Outline each Plasmodium vivax-infected red blood cell.
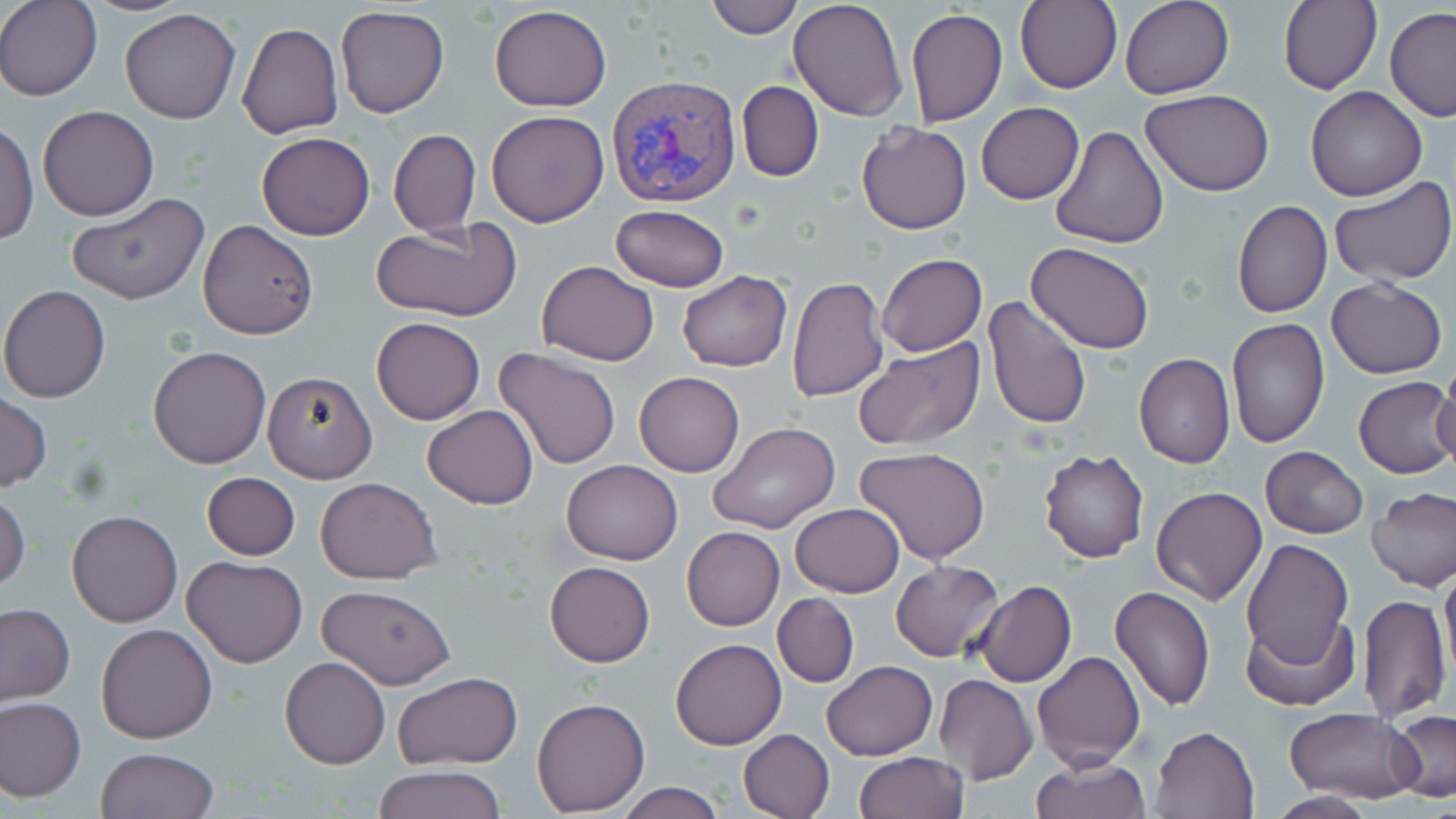
Approximate bounding boxes as (x1,y1)-(x2,y2) corner pairs in pixels.
Plasmodium vivax-infected red blood cells: (608,75)-(739,208).

slide-level diagnosis = Plasmodium vivax
field of view = single
uninfected red blood cell locations = approximate bounding boxes as (x1,y1)-(x2,y2) corner pairs in pixels: (0,0)-(101,101), (703,0)-(804,39), (788,0)-(909,121), (1120,0)-(1234,99), (1015,1)-(1122,94), (1279,1)-(1381,94), (336,5)-(450,118), (489,5)-(612,112), (1384,7)-(1456,122), (120,8)-(240,124), (906,9)-(1008,126), (238,21)-(345,140), (736,80)-(824,183), (1305,86)-(1428,201), (1141,90)-(1275,196), (976,103)-(1085,204), (38,105)-(160,220), (486,110)-(609,227), (0,118)-(38,248), (857,122)-(972,235), (1049,126)-(1168,249), (388,129)-(480,235), (256,132)-(375,241), (1330,176)-(1455,286), (66,192)-(210,307), (1232,200)-(1332,318), (612,205)-(730,292), (197,219)-(318,339), (370,223)-(521,320), (1026,241)-(1156,355), (877,253)-(986,357), (537,261)-(659,365), (678,271)-(791,371), (787,276)-(888,401), (1326,277)-(1448,379), (1,283)-(113,402), (981,295)-(1094,432), (1227,316)-(1330,449), (371,317)-(484,425), (854,336)-(985,451), (149,345)-(271,468), (493,347)-(622,472), (1134,354)-(1235,468), (1431,367)-(1456,473), (261,369)-(379,483), (633,371)-(745,476), (1353,375)-(1456,479), (0,392)-(51,493), (422,404)-(538,510), (710,422)-(841,533), (854,446)-(991,566), (1261,446)-(1368,539), (1039,449)-(1149,562), (560,460)-(684,565), (202,472)-(300,560), (315,477)-(442,584), (1151,487)-(1267,606), (1367,487)-(1456,592), (0,491)-(30,593), (790,504)-(905,596), (65,510)-(183,628), (682,527)-(785,631), (1241,539)-(1353,675), (182,556)-(309,668), (891,560)-(1003,662), (1440,560)-(1456,676), (545,561)-(655,667), (972,579)-(1076,688), (318,584)-(457,689), (1109,586)-(1216,711), (772,593)-(859,687), (1357,594)-(1450,721), (0,604)-(74,705), (1241,612)-(1357,712), (95,623)-(218,744), (670,640)-(786,751), (1031,650)-(1144,772), (279,656)-(390,769), (821,659)-(937,761), (393,672)-(523,769), (934,675)-(1037,785), (1,696)-(86,800), (532,697)-(650,815), (1286,707)-(1424,803), (1386,711)-(1456,804), (1151,725)-(1261,817), (737,729)-(834,819), (95,747)-(218,819), (854,752)-(969,819), (1031,755)-(1150,818), (372,766)-(504,819), (616,781)-(725,819), (1263,792)-(1378,819)
preparation = thin blood smear
stain = May-Grünwald-Giemsa
image size = 1456×819 pixels
magnification = 1000x
modality = light microscopy